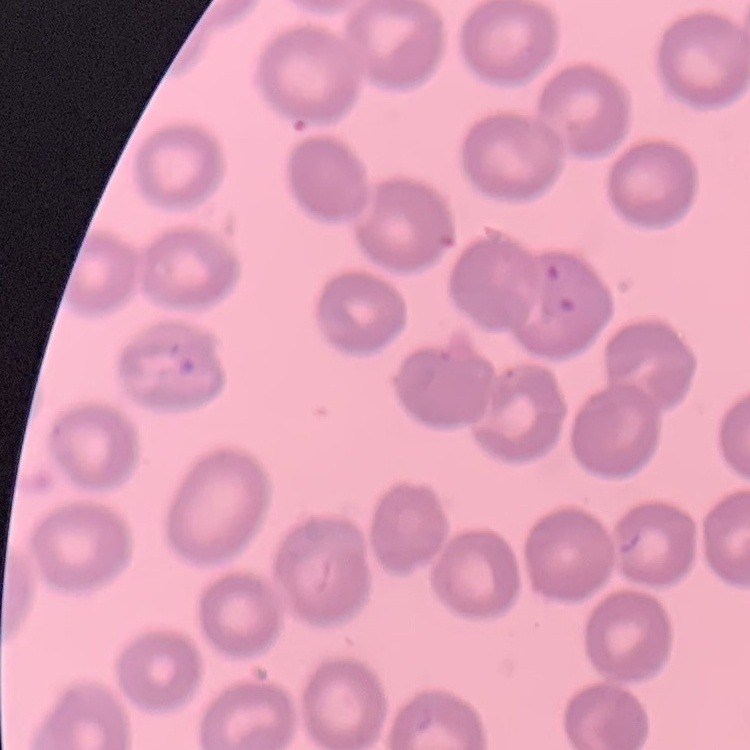

Summary:
  - Red blood cell morphology: no rouleaux formation
  - Preparation: thin blood film
  - Image type: one tile cut from a larger photomicrograph
  - Stain: Field's or Giemsa